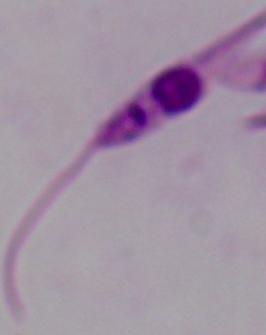
A Leishmania parasite is seen. Micrograph. 1000x magnification.